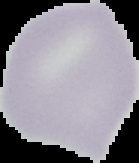
image size = 139×163 pixels
image type = segmented cell region with the area outside set to black
malaria status = uninfected
preparation = thin blood film